Assess this cell for malaria.
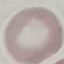
Uninfected.

Summary:
  - Stain: Giemsa
  - Image type: automatically extracted cell patch, resized to 64 × 64 pixels
  - Preparation: thin blood smear
  - Capture: smartphone camera at the microscope eyepiece